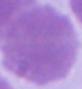
{
  "magnification": "1000x",
  "identification": "red blood cell",
  "modality": "micrograph"
}